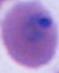
identification: Plasmodium
modality: micrograph
magnification: 400x or 1000x